Identify the parasite.
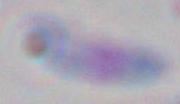

This is Toxoplasma gondii.

Summary:
  - Magnification: 1000x
  - Modality: photomicrograph